Outline each Plasmodium falciparum-infected red blood cell.
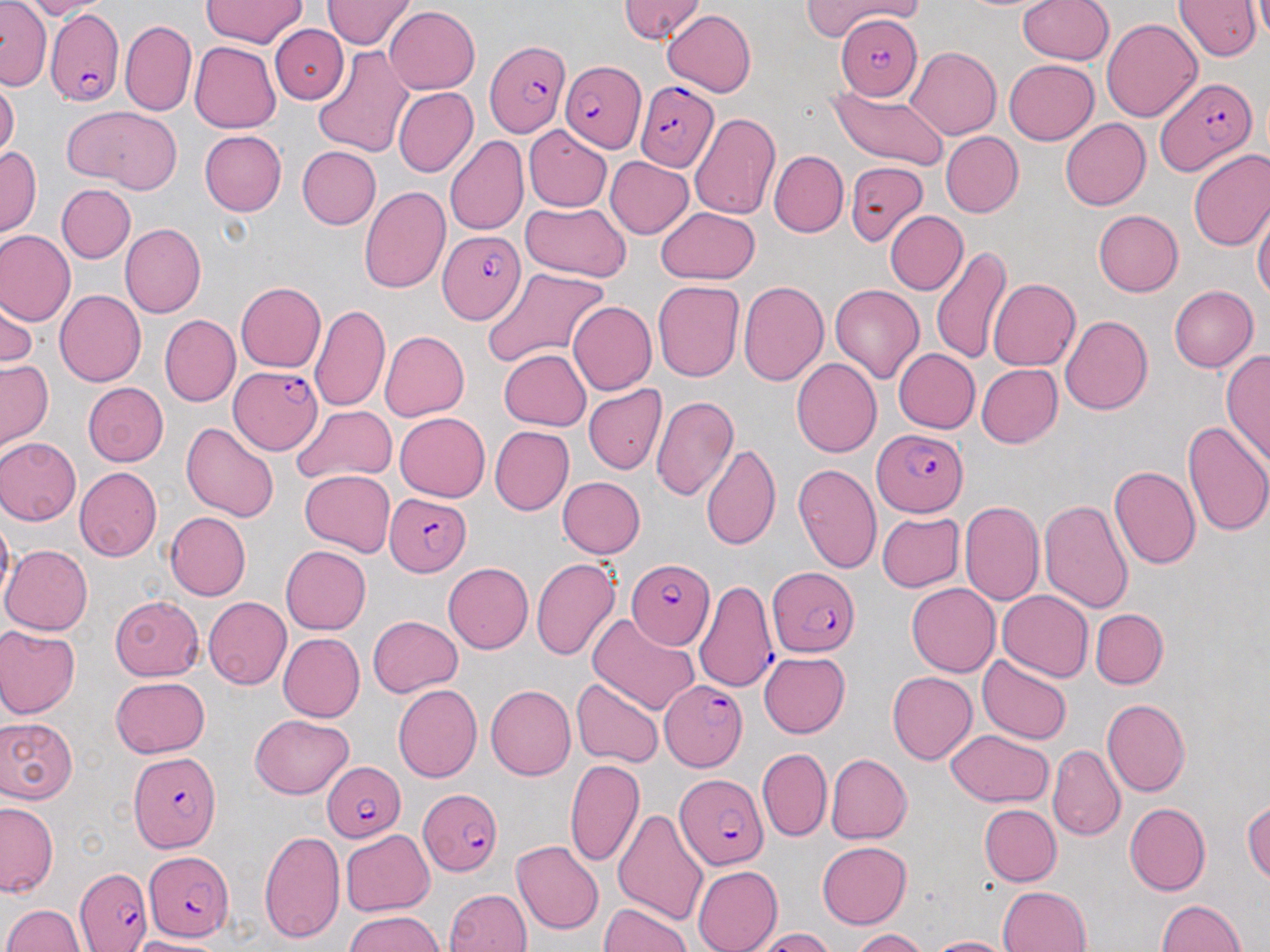

Approximate bounding boxes as (x1,y1)-(x2,y2) corner pairs in pixels.
Plasmodium falciparum-infected red blood cells: (44,9)-(123,105), (832,18)-(925,99), (486,42)-(567,136), (560,57)-(645,151), (1156,77)-(1258,175), (635,79)-(718,171), (438,231)-(525,324), (229,365)-(323,455), (872,428)-(968,516), (385,491)-(473,576), (626,560)-(715,651), (769,568)-(858,655), (691,580)-(776,691), (660,678)-(746,771), (129,753)-(221,853), (322,762)-(404,842), (679,774)-(768,869), (418,789)-(501,879), (142,852)-(235,940), (76,867)-(152,952).

slide-level diagnosis = Plasmodium falciparum
uninfected red blood cell locations = approximate bounding boxes as (x1,y1)-(x2,y2) corner pairs in pixels: (22,0)-(116,19), (618,0)-(705,43), (801,0)-(926,41), (1019,0)-(1114,64), (1173,0)-(1261,61), (202,1)-(308,48), (322,1)-(415,49), (0,3)-(52,89), (384,5)-(480,95), (662,9)-(756,98), (1100,18)-(1201,122), (120,20)-(196,116), (270,24)-(349,105), (190,42)-(280,133), (311,44)-(413,158), (906,46)-(1002,140), (1004,59)-(1098,145), (0,80)-(20,162), (392,87)-(478,177), (830,87)-(949,170), (61,105)-(182,195), (690,112)-(781,220), (1060,118)-(1151,210), (524,124)-(612,211), (199,129)-(286,215), (941,132)-(1023,217), (445,135)-(528,236), (296,146)-(381,229), (0,147)-(42,237), (1187,149)-(1270,251), (769,150)-(848,237), (604,156)-(694,239), (846,161)-(927,246), (57,184)-(135,263), (359,186)-(450,295), (520,202)-(632,282), (1253,203)-(1270,304), (653,206)-(760,285), (884,210)-(967,295), (1094,210)-(1183,297), (120,223)-(206,318), (0,230)-(75,325), (930,245)-(1013,364), (483,267)-(609,368), (988,278)-(1080,370), (652,279)-(745,382), (738,280)-(828,387), (235,282)-(326,371), (829,283)-(924,385), (1169,285)-(1258,372), (0,290)-(37,372), (54,290)-(145,386), (568,300)-(656,395), (309,304)-(390,413), (159,314)-(240,406), (1059,315)-(1152,415), (380,331)-(469,421), (893,348)-(981,433), (1220,348)-(1270,471), (499,349)-(591,431), (791,357)-(881,457), (895,357)-(1064,438), (0,359)-(53,452), (976,364)-(1063,448), (82,382)-(169,467), (583,384)-(667,475), (650,394)-(738,501), (291,403)-(397,483), (393,412)-(490,501), (1181,419)-(1270,539), (180,421)-(280,522), (489,426)-(574,516), (0,436)-(82,525), (702,443)-(782,549), (791,461)-(882,575), (1108,465)-(1201,569), (75,467)-(161,561), (298,469)-(395,558), (557,477)-(646,559), (959,500)-(1044,606), (1039,500)-(1134,616), (0,511)-(14,605), (165,511)-(251,600), (878,511)-(964,592), (1,544)-(92,635), (281,545)-(370,634), (530,558)-(622,661), (443,562)-(533,654), (907,584)-(1000,677), (997,590)-(1093,681), (110,597)-(204,681), (203,597)-(291,689), (1090,609)-(1168,689), (587,612)-(701,716), (368,616)-(463,697), (0,625)-(80,719), (278,633)-(365,722), (759,652)-(851,737), (977,655)-(1071,744), (887,672)-(978,765), (111,677)-(209,757), (571,678)-(665,767), (486,684)-(576,781), (393,685)-(483,783), (1101,698)-(1190,798), (250,714)-(355,799), (0,718)-(77,802), (946,729)-(1053,805), (1048,744)-(1126,841), (757,748)-(830,841), (826,753)-(912,843), (565,759)-(645,868), (1243,798)-(1270,885), (0,801)-(58,898), (1124,803)-(1211,896), (979,804)-(1061,886), (614,810)-(709,926), (341,829)-(434,915), (260,830)-(345,944), (512,840)-(604,935), (817,842)-(912,928), (344,861)-(439,948), (693,865)-(781,952), (998,885)-(1091,952), (445,888)-(533,952), (1156,899)-(1247,951), (599,903)-(691,952), (3,904)-(84,952), (344,909)-(445,952), (750,927)-(837,952), (852,928)-(930,952), (926,936)-(1017,952), (127,937)-(230,952)
preparation = thin blood smear
image size = 1270×952 pixels
stain = May-Grünwald-Giemsa
modality = light microscopy
magnification = 1000x
field of view = single